Point out each Plasmodium parasite.
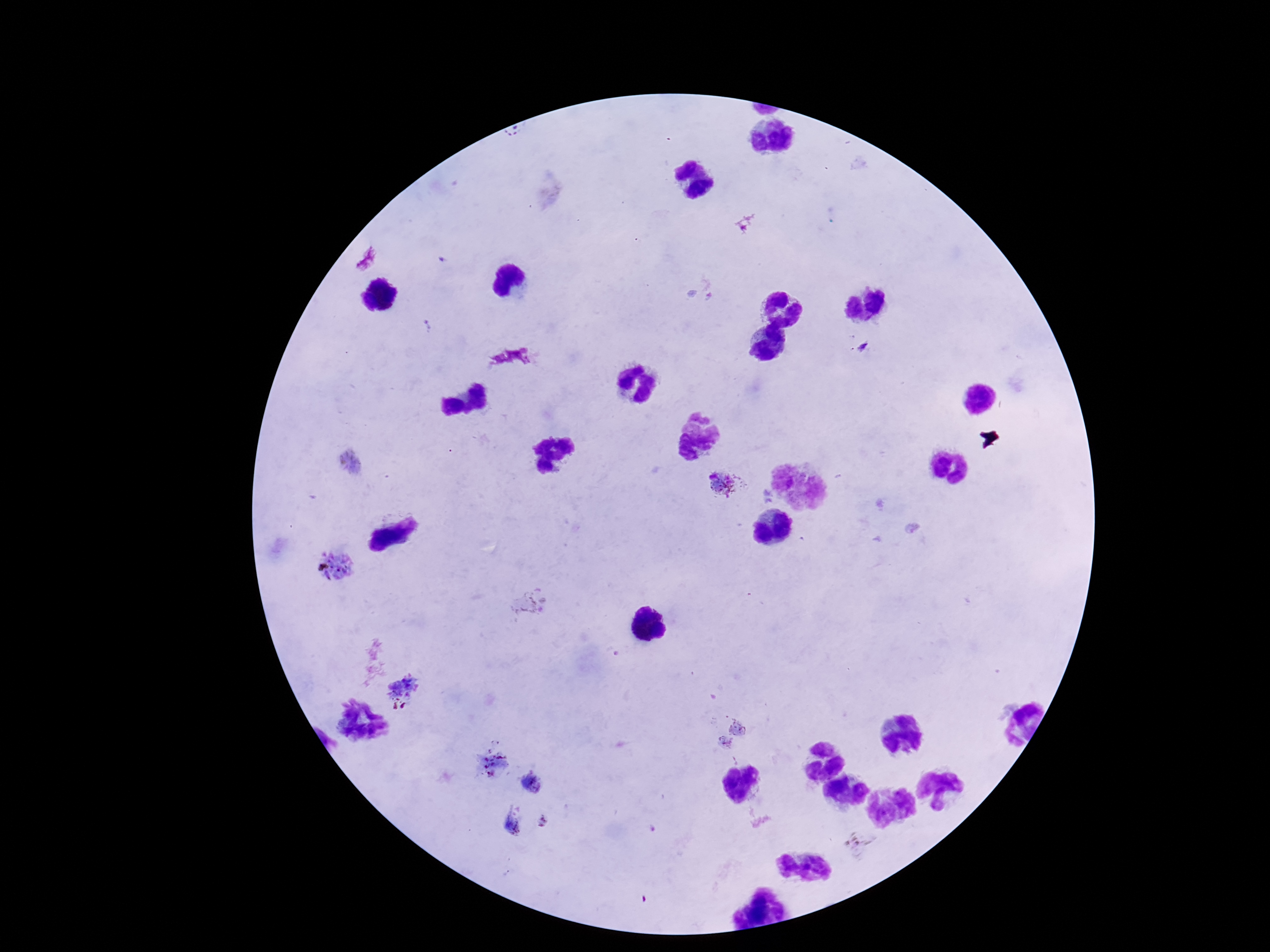
Approximate centers as {x, y} in pixels.
Plasmodium parasites: {862, 347}, {352, 461}, {724, 485}, {338, 566}, {529, 602}, {400, 691}, {738, 728}, {725, 744}, {493, 762}, {533, 781}, {514, 821}, {544, 821}, {861, 842}.

Patient malaria status: infected. 100x magnification. Image is 1270×952 pixels. One field from this slide. Thick peripheral-blood smear. Smartphone photograph taken through the microscope eyepiece. Giemsa stain.